Outline each blood parasite and name the species.
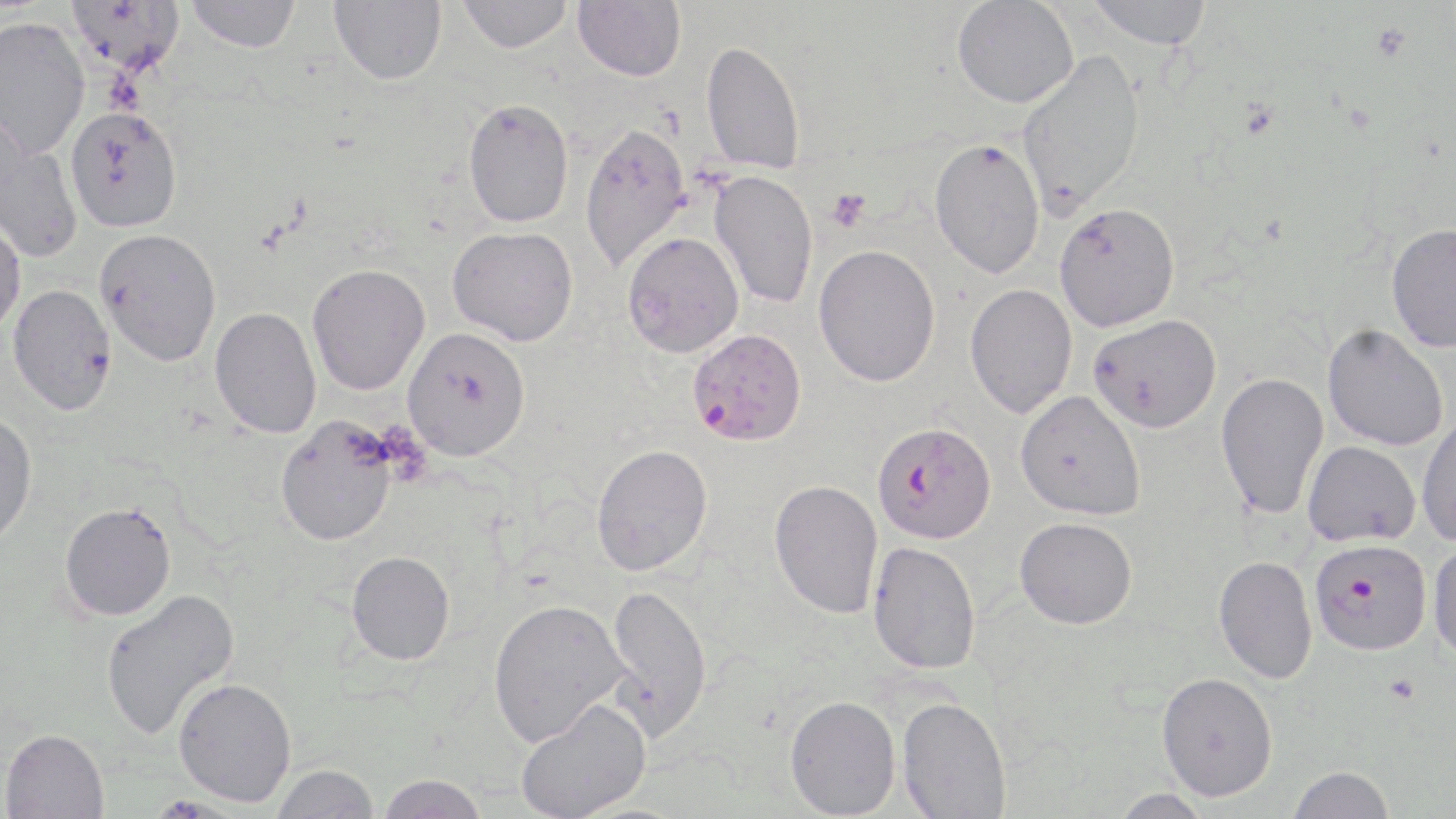
Approximate bounding boxes as (x1,y1)-(x2,y2) corner pairs in pixels.
Plasmodium falciparum-infected red blood cells: (687,328)-(806,446), (872,421)-(996,543), (1308,537)-(1432,655).
No Plasmodium ovale, Plasmodium malariae, Plasmodium vivax, Babesia divergens, or Trypanosoma brucei observed.

Summary:
  - Uninfected red blood cell locations: (65,0)-(185,78), (186,0)-(302,53), (330,0)-(446,85), (457,0)-(573,53), (1085,0)-(1213,49), (573,1)-(686,82), (952,1)-(1078,108), (0,16)-(91,160), (701,40)-(806,175), (1016,50)-(1145,219), (463,98)-(574,228), (64,105)-(183,233), (579,121)-(691,273), (0,122)-(82,265), (929,137)-(1045,279), (709,170)-(819,309), (1054,203)-(1180,332), (0,215)-(26,338), (1385,222)-(1456,353), (447,226)-(578,346), (95,228)-(222,366), (622,231)-(744,357), (813,244)-(941,387), (307,263)-(430,395), (964,283)-(1078,418), (7,284)-(118,416), (209,307)-(322,439), (1088,314)-(1222,432), (1322,323)-(1449,451), (402,327)-(531,461), (1215,372)-(1329,520), (1015,390)-(1146,521), (0,412)-(38,548), (1416,413)-(1456,546), (275,417)-(398,546), (1303,441)-(1421,547), (591,443)-(713,576), (769,479)-(883,619), (59,502)-(176,620), (1015,517)-(1137,629), (1428,539)-(1456,667), (868,540)-(981,674), (346,550)-(456,665), (1213,555)-(1317,684), (605,583)-(712,742), (99,589)-(240,739), (487,598)-(630,747), (1157,672)-(1278,801), (173,677)-(297,807), (784,694)-(901,818), (897,695)-(1012,819), (515,697)-(652,819), (1,728)-(109,818), (272,763)-(379,819), (1287,765)-(1395,819), (377,774)-(489,818), (1111,788)-(1215,818)
  - Platelet locations: (826,188)-(872,233)
  - Slide-level diagnosis: Plasmodium falciparum
  - Image size: 1456×819 pixels
  - Stain: May-Grünwald-Giemsa
  - Field of view: one of a larger specimen
  - Magnification: 1000x
  - Modality: optical microscopy
  - Preparation: thin blood film